Classify this cell by malaria status.
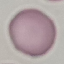

Uninfected.

Photographed with a smartphone camera at the microscope eyepiece. Cell patch, automatically extracted from a larger field of view and resized to 64 × 64 pixels. Giemsa-stained preparation. Thin smear of blood.